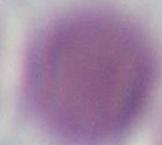

Summary:
  - Magnification: 1000x
  - Identification: red blood cell
  - Modality: micrograph